Name the blood parasite species.
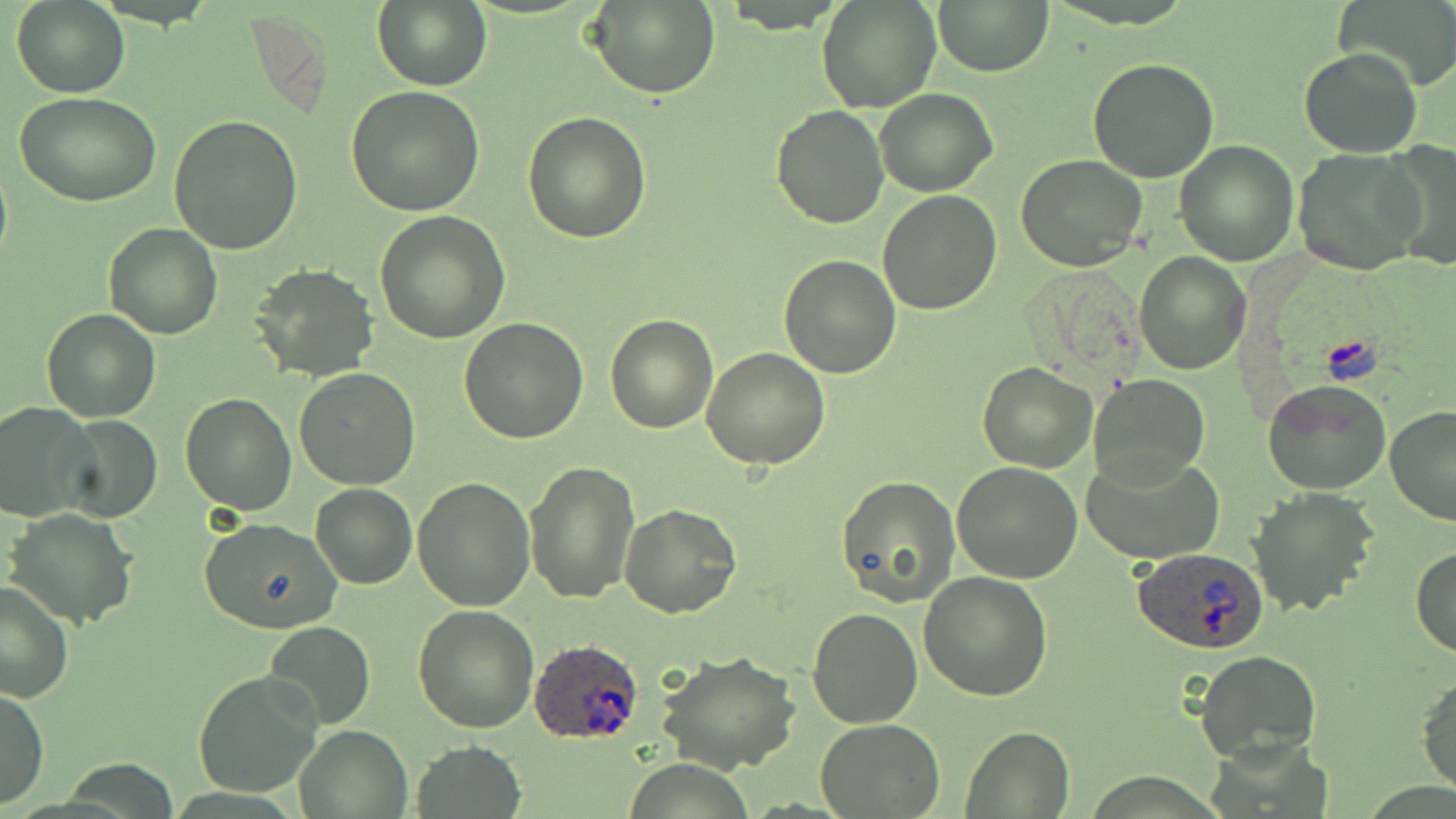

Plasmodium ovale.

Summary:
  - Coordinate format: approximate bounding boxes as (x1,y1)-(x2,y2) corner pairs in pixels
  - Plasmodium ovale-infected red blood cell locations: (1132,546)-(1269,654), (529,636)-(645,744)
  - Uninfected red blood cell locations: (816,0)-(942,114), (933,0)-(1053,77), (1334,0)-(1456,91), (10,1)-(130,97), (371,1)-(491,91), (586,1)-(720,99), (1299,47)-(1422,158), (1086,58)-(1219,183), (346,84)-(485,214), (875,89)-(998,196), (17,93)-(160,206), (770,104)-(890,229), (522,110)-(652,244), (170,114)-(304,254), (1173,139)-(1298,265), (1379,140)-(1456,271), (1293,148)-(1425,275), (1015,156)-(1148,271), (878,190)-(1001,315), (375,211)-(511,343), (104,222)-(223,340), (1135,251)-(1248,374), (778,254)-(901,378), (250,264)-(378,383), (41,307)-(161,422), (605,314)-(719,434), (459,316)-(587,443), (701,346)-(830,471), (978,362)-(1098,473), (293,369)-(422,490), (1088,374)-(1210,483), (1262,380)-(1391,496), (180,392)-(298,513), (0,401)-(95,521), (1384,406)-(1456,526), (57,415)-(163,524), (1081,450)-(1225,565), (523,459)-(640,604), (951,462)-(1083,585), (835,474)-(960,607), (412,476)-(538,611), (311,484)-(417,588), (1245,487)-(1381,618), (619,503)-(742,620), (6,509)-(138,628), (198,518)-(343,635), (1410,545)-(1456,658), (919,571)-(1053,702), (0,581)-(74,704), (412,603)-(541,733), (808,609)-(924,729), (263,621)-(377,731), (1193,648)-(1324,768), (656,649)-(802,775), (192,668)-(325,800), (1416,670)-(1456,798), (1,687)-(48,811), (815,717)-(945,816), (292,724)-(412,818), (959,726)-(1074,817), (410,740)-(527,818)
  - Field of view: single
  - Image size: 1456×819 pixels
  - Modality: light microscopy
  - Preparation: thin blood smear
  - Stain: May-Grünwald-Giemsa
  - Magnification: 1000x